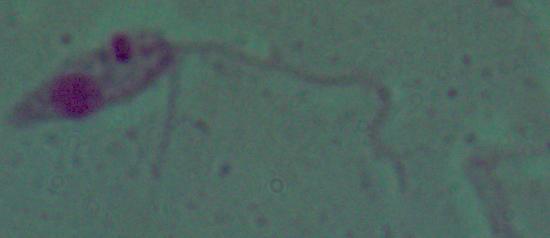
Summary:
  - Modality: photomicrograph
  - Magnification: 1000x
  - Identification: Leishmania